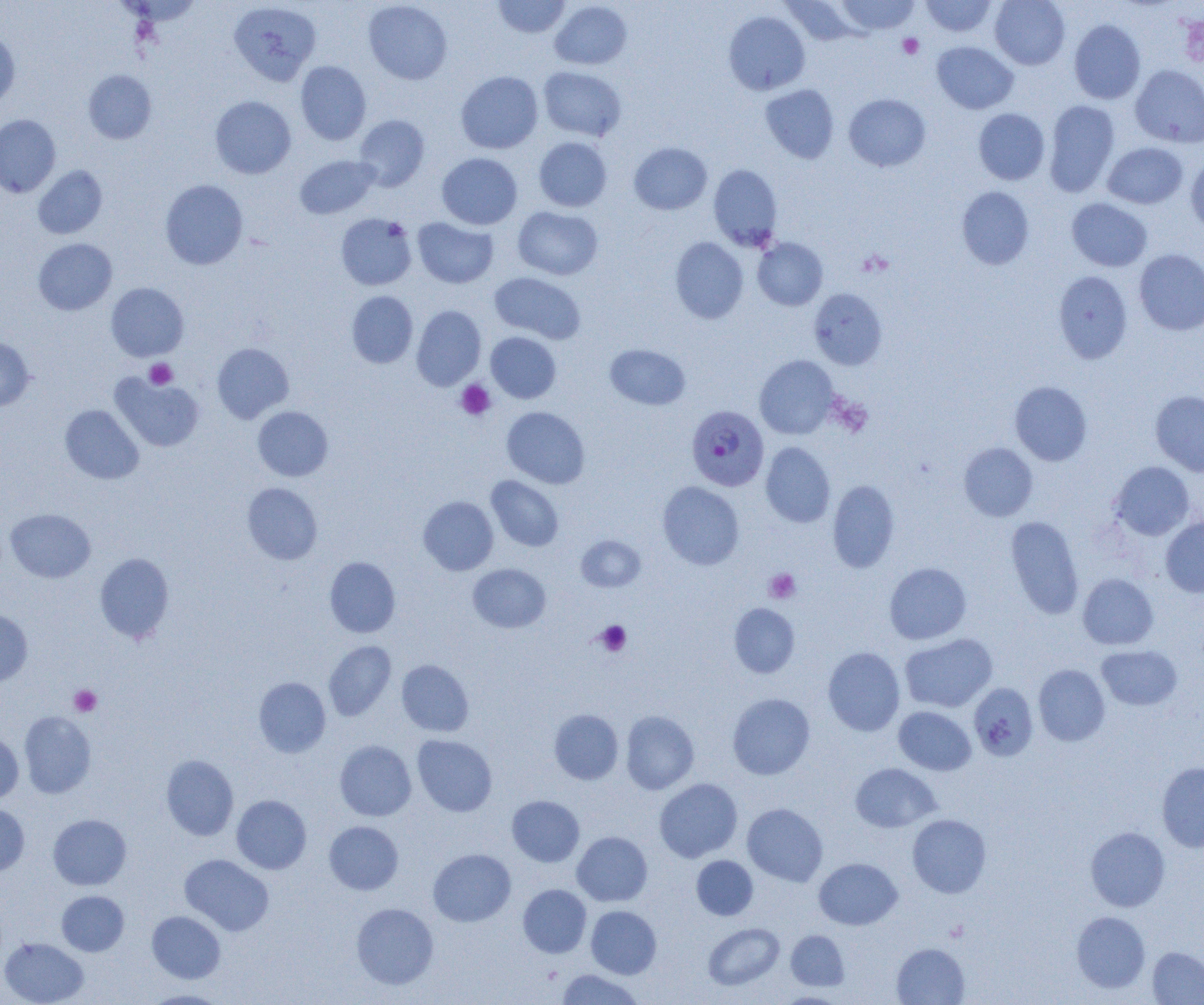
Summary:
  - Coordinate format: approximate bounding boxes as named x1/y1/x2/y2 corners in pixels
  - Plasmodium falciparum-infected red blood cell locations: (x1=688, y1=408, x2=772, y2=492)
  - Uninfected red blood cell locations: (x1=492, y1=0, x2=570, y2=38), (x1=834, y1=0, x2=920, y2=35), (x1=920, y1=0, x2=998, y2=37), (x1=990, y1=0, x2=1070, y2=69), (x1=228, y1=1, x2=321, y2=86), (x1=363, y1=1, x2=453, y2=84), (x1=550, y1=1, x2=632, y2=70), (x1=781, y1=1, x2=863, y2=47), (x1=1178, y1=10, x2=1204, y2=70), (x1=723, y1=11, x2=810, y2=95), (x1=1069, y1=19, x2=1146, y2=104), (x1=0, y1=31, x2=20, y2=109), (x1=932, y1=41, x2=1018, y2=114), (x1=295, y1=61, x2=371, y2=145), (x1=1131, y1=64, x2=1204, y2=148), (x1=538, y1=66, x2=626, y2=141), (x1=83, y1=69, x2=157, y2=144), (x1=456, y1=71, x2=543, y2=153), (x1=760, y1=84, x2=839, y2=163), (x1=844, y1=93, x2=931, y2=172), (x1=210, y1=96, x2=296, y2=179), (x1=1043, y1=100, x2=1120, y2=197), (x1=973, y1=108, x2=1050, y2=185), (x1=0, y1=114, x2=60, y2=197), (x1=354, y1=115, x2=430, y2=190), (x1=534, y1=137, x2=612, y2=212), (x1=629, y1=142, x2=712, y2=215), (x1=1103, y1=143, x2=1188, y2=209), (x1=437, y1=153, x2=522, y2=229), (x1=1185, y1=154, x2=1204, y2=234), (x1=295, y1=155, x2=380, y2=219), (x1=708, y1=164, x2=782, y2=250), (x1=33, y1=165, x2=107, y2=239), (x1=160, y1=180, x2=248, y2=269), (x1=957, y1=186, x2=1034, y2=270), (x1=1067, y1=198, x2=1152, y2=271), (x1=513, y1=206, x2=603, y2=280), (x1=336, y1=213, x2=417, y2=290), (x1=412, y1=217, x2=498, y2=288), (x1=670, y1=237, x2=748, y2=323), (x1=753, y1=237, x2=828, y2=310), (x1=33, y1=238, x2=117, y2=315), (x1=1134, y1=249, x2=1204, y2=335), (x1=1053, y1=271, x2=1132, y2=363), (x1=490, y1=272, x2=586, y2=343), (x1=106, y1=283, x2=189, y2=361), (x1=809, y1=288, x2=887, y2=370), (x1=346, y1=291, x2=418, y2=368), (x1=411, y1=305, x2=486, y2=390), (x1=486, y1=332, x2=561, y2=403), (x1=0, y1=337, x2=35, y2=411), (x1=212, y1=343, x2=294, y2=423), (x1=605, y1=344, x2=690, y2=410), (x1=754, y1=355, x2=839, y2=439), (x1=112, y1=373, x2=204, y2=452), (x1=1010, y1=381, x2=1092, y2=465), (x1=1150, y1=390, x2=1204, y2=476), (x1=60, y1=405, x2=144, y2=484), (x1=252, y1=406, x2=333, y2=481), (x1=502, y1=406, x2=589, y2=488), (x1=761, y1=442, x2=835, y2=528), (x1=959, y1=442, x2=1038, y2=521), (x1=1110, y1=461, x2=1194, y2=540), (x1=486, y1=475, x2=564, y2=551), (x1=827, y1=480, x2=900, y2=572), (x1=242, y1=482, x2=323, y2=565), (x1=658, y1=482, x2=744, y2=569), (x1=418, y1=496, x2=499, y2=575), (x1=6, y1=508, x2=95, y2=582), (x1=1005, y1=515, x2=1084, y2=619), (x1=1161, y1=516, x2=1204, y2=597), (x1=576, y1=535, x2=646, y2=592), (x1=94, y1=553, x2=174, y2=643), (x1=324, y1=557, x2=400, y2=637), (x1=884, y1=562, x2=971, y2=644), (x1=468, y1=563, x2=551, y2=633), (x1=1078, y1=574, x2=1159, y2=650), (x1=729, y1=603, x2=800, y2=677), (x1=0, y1=610, x2=33, y2=686), (x1=900, y1=633, x2=997, y2=712), (x1=323, y1=640, x2=396, y2=720), (x1=1097, y1=645, x2=1182, y2=710), (x1=823, y1=647, x2=905, y2=736), (x1=396, y1=660, x2=474, y2=736), (x1=1033, y1=664, x2=1110, y2=746), (x1=253, y1=677, x2=331, y2=757), (x1=969, y1=683, x2=1038, y2=761), (x1=727, y1=693, x2=815, y2=779), (x1=894, y1=706, x2=976, y2=775), (x1=549, y1=709, x2=623, y2=784), (x1=621, y1=710, x2=699, y2=794), (x1=19, y1=711, x2=96, y2=798), (x1=0, y1=732, x2=23, y2=804), (x1=412, y1=735, x2=497, y2=816), (x1=335, y1=740, x2=416, y2=821), (x1=161, y1=755, x2=239, y2=840), (x1=1156, y1=762, x2=1204, y2=852), (x1=850, y1=763, x2=941, y2=833), (x1=654, y1=778, x2=742, y2=862), (x1=232, y1=795, x2=311, y2=874), (x1=507, y1=795, x2=584, y2=866), (x1=0, y1=803, x2=30, y2=876), (x1=742, y1=803, x2=828, y2=886), (x1=48, y1=814, x2=131, y2=890), (x1=907, y1=814, x2=991, y2=898), (x1=324, y1=821, x2=403, y2=895), (x1=1085, y1=827, x2=1170, y2=912), (x1=572, y1=831, x2=652, y2=906), (x1=428, y1=848, x2=515, y2=926), (x1=180, y1=854, x2=274, y2=935), (x1=692, y1=855, x2=758, y2=920), (x1=814, y1=858, x2=902, y2=930), (x1=518, y1=884, x2=591, y2=958), (x1=57, y1=890, x2=129, y2=956), (x1=351, y1=903, x2=438, y2=989), (x1=586, y1=905, x2=661, y2=978), (x1=147, y1=911, x2=226, y2=983), (x1=1072, y1=911, x2=1150, y2=993), (x1=703, y1=923, x2=784, y2=990), (x1=786, y1=930, x2=849, y2=990), (x1=0, y1=937, x2=88, y2=1005), (x1=891, y1=943, x2=969, y2=1005), (x1=1147, y1=947, x2=1204, y2=1004), (x1=556, y1=969, x2=645, y2=1005), (x1=142, y1=990, x2=228, y2=1005), (x1=774, y1=992, x2=848, y2=1004)
  - Platelet locations: (x1=898, y1=34, x2=924, y2=59), (x1=144, y1=359, x2=177, y2=389), (x1=455, y1=380, x2=496, y2=420), (x1=765, y1=568, x2=801, y2=603), (x1=594, y1=620, x2=631, y2=656), (x1=70, y1=685, x2=101, y2=716)
  - Slide-level diagnosis: Plasmodium falciparum
  - Image size: 1204×1005 pixels
  - Modality: light microscopy
  - Field of view: one of a larger specimen
  - Magnification: 1000x
  - Preparation: thin blood smear